Assess this cell for malaria.
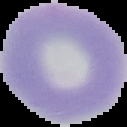

Uninfected.

image size = 127×127 pixels
preparation = thin blood film
image type = cell region segmented out of the field of view; surrounding area masked to black